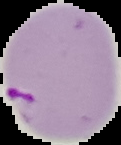
Summary:
  - Image size: 121×145 pixels
  - Image type: segmented cell region on a black background
  - Preparation: thin blood film
  - Result: malaria parasites identified